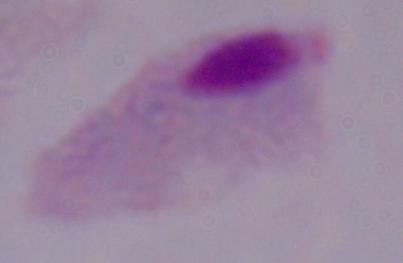

magnification: 1000x
identification: trichomonad
modality: photomicrograph